Name the blood parasite species.
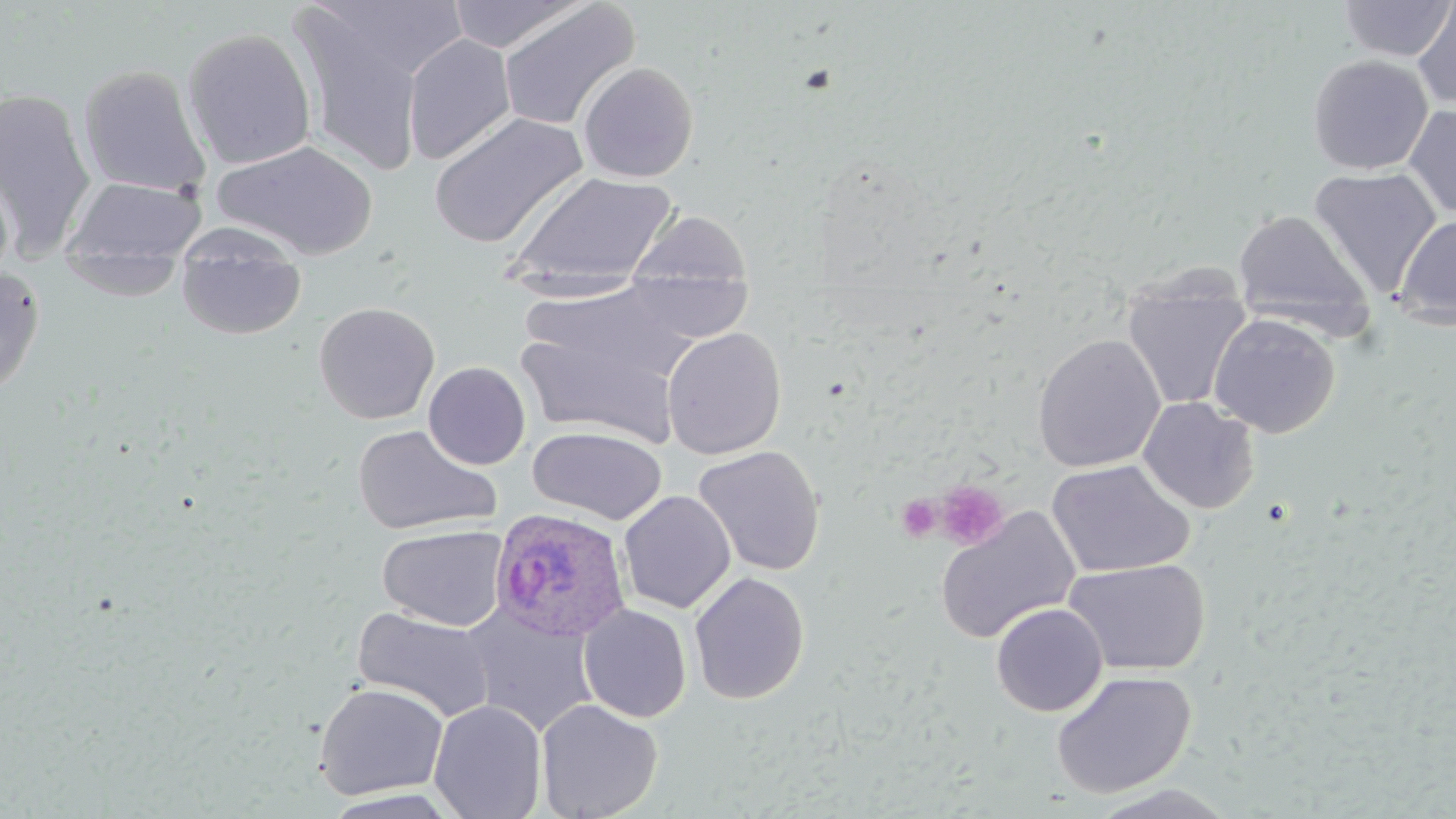
Plasmodium ovale.

platelet_locations: 'approximate bounding boxes as (x1,y1)-(x2,y2) corner pairs in pixels: (935,479)-(1009,550), (895,493)-(943,543)'
stain: May-Grünwald-Giemsa
preparation: thin blood film
uninfected_red_blood_cell_locations: 'approximate bounding boxes as (x1,y1)-(x2,y2) corner pairs in pixels: (445,0)-(588,53), (1337,0)-(1455,62), (497,1)-(640,133), (1413,3)-(1456,109), (289,4)-(432,176), (181,26)-(317,170), (402,33)-(516,164), (1308,54)-(1433,174), (577,61)-(699,182), (77,64)-(211,197), (0,87)-(96,256), (1403,105)-(1456,218), (428,112)-(586,248), (213,140)-(378,261), (1308,168)-(1441,297), (507,170)-(679,287), (0,173)-(15,287), (62,176)-(207,265), (1233,209)-(1372,332), (628,210)-(753,295), (1394,215)-(1456,329), (177,243)-(307,341), (61,252)-(186,301), (0,266)-(45,397), (624,268)-(755,344), (1122,279)-(1251,411), (521,284)-(693,386), (313,301)-(440,424), (1209,313)-(1340,438), (512,325)-(684,449), (662,327)-(786,460), (1032,335)-(1165,473), (423,361)-(531,470), (1138,397)-(1260,514), (351,424)-(501,536), (528,426)-(667,524), (693,445)-(825,576), (1046,459)-(1196,579), (618,490)-(736,614), (934,505)-(1080,645), (377,523)-(509,631), (1063,558)-(1211,676), (689,571)-(811,705), (991,603)-(1108,717), (579,604)-(692,723), (464,605)-(600,736), (352,606)-(496,722), (1051,670)-(1196,798), (313,682)-(449,799), (536,698)-(663,819), (429,699)-(546,819), (1087,784)-(1239,819), (320,789)-(461,817)'
field_of_view: single
image_size: 1456×819 pixels
magnification: 1000x
plasmodium_ovale_infected_red_blood_cell_locations: 'approximate bounding boxes as (x1,y1)-(x2,y2) corner pairs in pixels: (490,507)-(631,643)'
modality: light microscopy